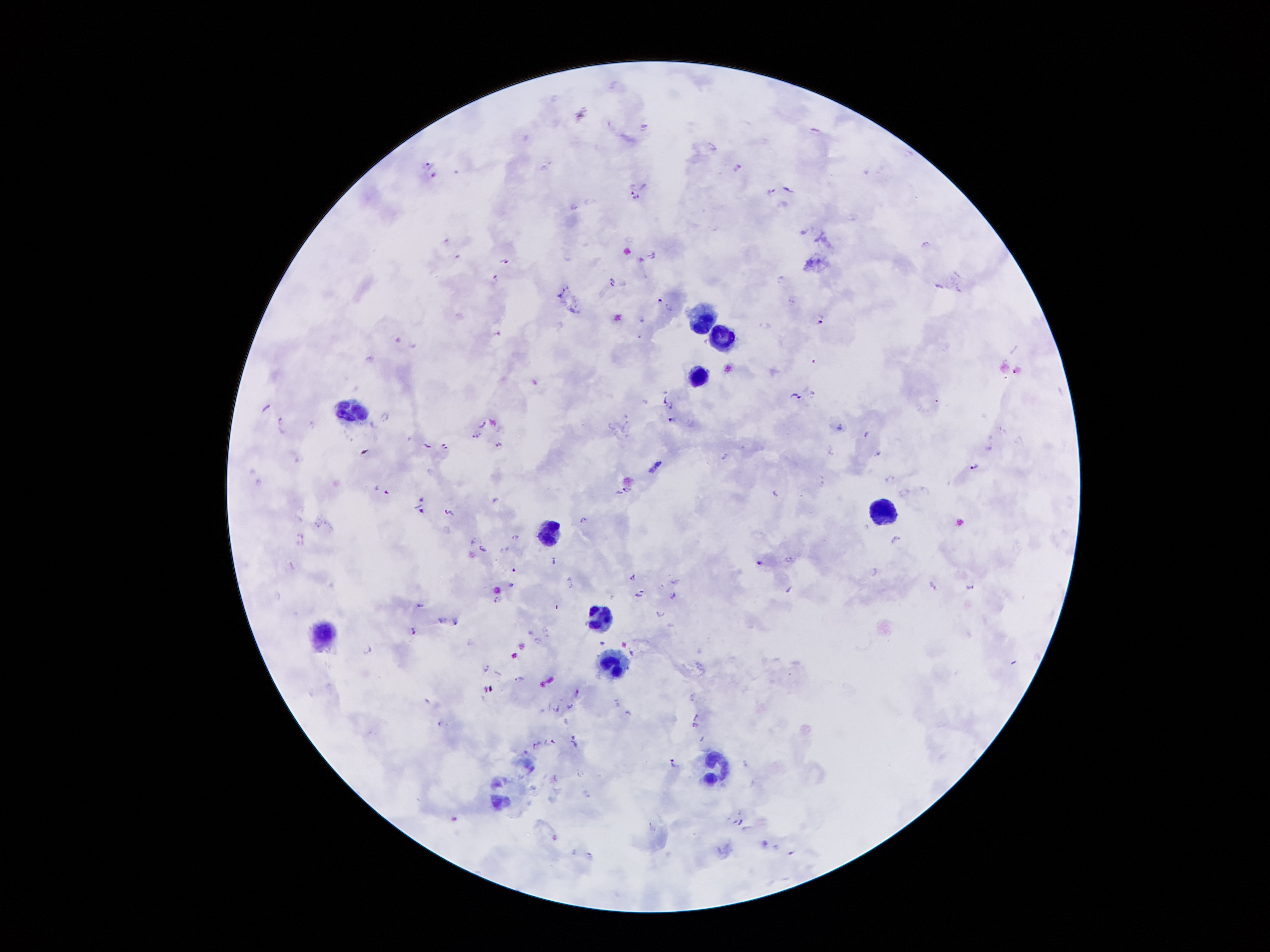

coordinate format = approximate centers as (x, y) in pixels
leukocyte locations = (704, 317), (724, 336), (695, 376), (351, 411), (883, 512), (545, 530), (602, 619), (321, 637), (613, 663), (717, 767)
Plasmodium parasite locations = (643, 124), (814, 130), (427, 164), (738, 166), (768, 190), (788, 190), (636, 195), (574, 206), (444, 240), (924, 244), (650, 254), (457, 257), (503, 261), (494, 279), (782, 279), (611, 281), (938, 286), (958, 289), (658, 297), (791, 300), (669, 307), (639, 319), (821, 320), (497, 330), (396, 340), (414, 345), (795, 395), (669, 405), (266, 408), (279, 418), (385, 418), (667, 418), (481, 423), (311, 425), (612, 427), (838, 427), (624, 428), (864, 434), (475, 435), (497, 443), (426, 444), (444, 445), (877, 453), (726, 455), (974, 465), (257, 481), (625, 489), (385, 491), (420, 498), (496, 499), (421, 508), (450, 513), (581, 519), (318, 525), (516, 536), (472, 540), (894, 540), (481, 548), (788, 559), (551, 560), (759, 562), (633, 577), (509, 584), (933, 584), (970, 586), (638, 594), (672, 595), (495, 599), (420, 605), (661, 614), (441, 621), (456, 621), (413, 628), (368, 647), (485, 667), (519, 679), (569, 706), (557, 708), (628, 712), (694, 724), (551, 741), (572, 742), (535, 744), (672, 762), (589, 856)
field of view = one from this slide
magnification = 100x
stain = Giemsa
image size = 1270×952 pixels
patient malaria status = positive for Plasmodium falciparum
capture = smartphone through the microscope eyepiece
preparation = thick blood smear